Assess this cell for malaria.
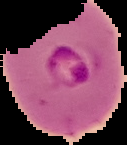
Parasitized.

{
  "image_size": "127×145 pixels",
  "preparation": "thin blood film",
  "image_type": "segmented cell region on a black background"
}